State which parasite is depicted.
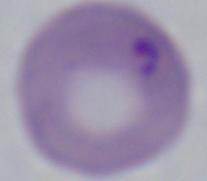

This is Babesia.

magnification: 1000x
modality: micrograph